Assess the morphology of the red blood cells.
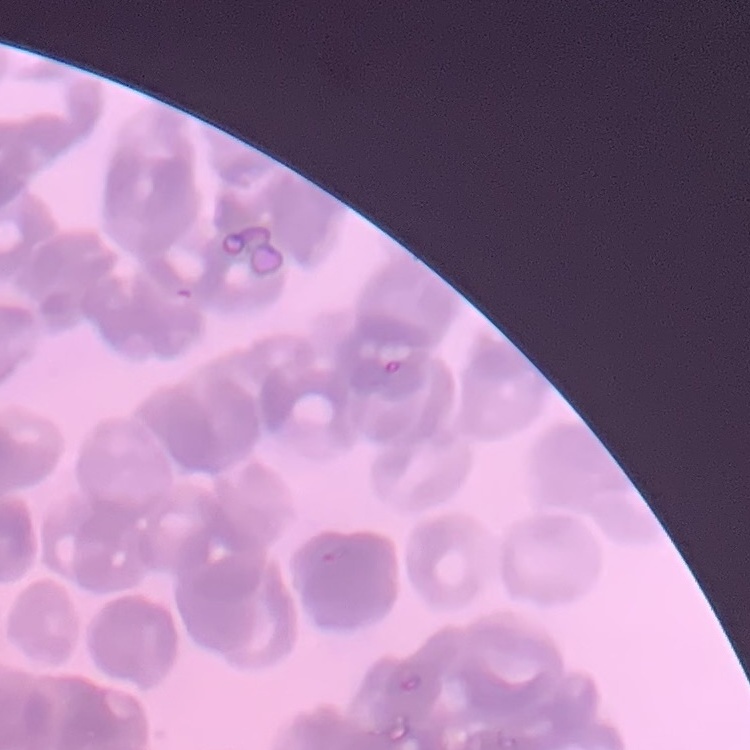
They show rouleaux formation.

One tile cut from a larger photomicrograph. Thin blood film. Stained with either Field's or Giemsa.